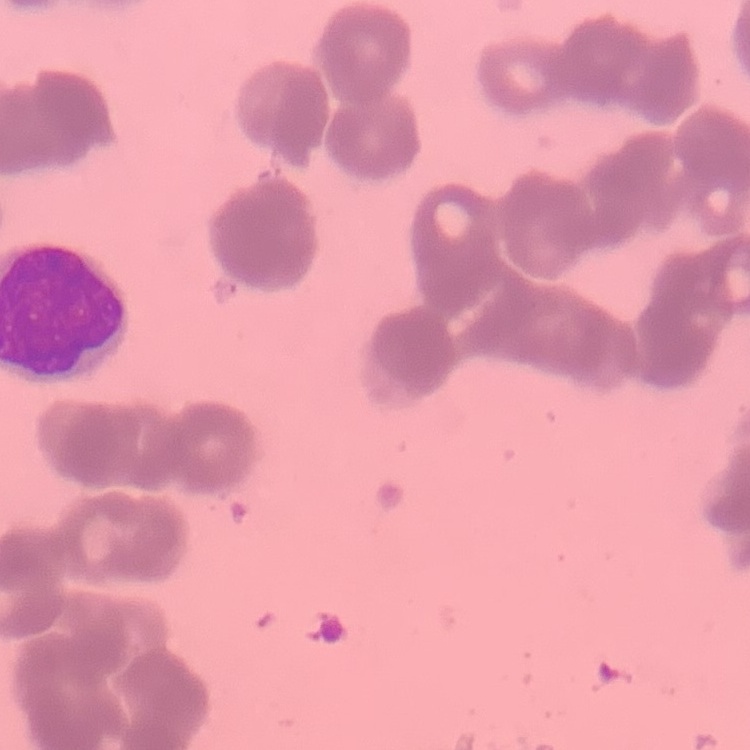
erythrocyte morphology = rouleaux formation
preparation = thin blood film
stain = Field's or Giemsa
image type = one tile cut from a larger photomicrograph